Report the malaria status of this cell.
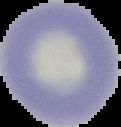

It is uninfected.

Image is 121×127 pixels. Cell region segmented out of the field of view; the surrounding area is masked to black. From a thin blood film.